Locate and identify every blood parasite.
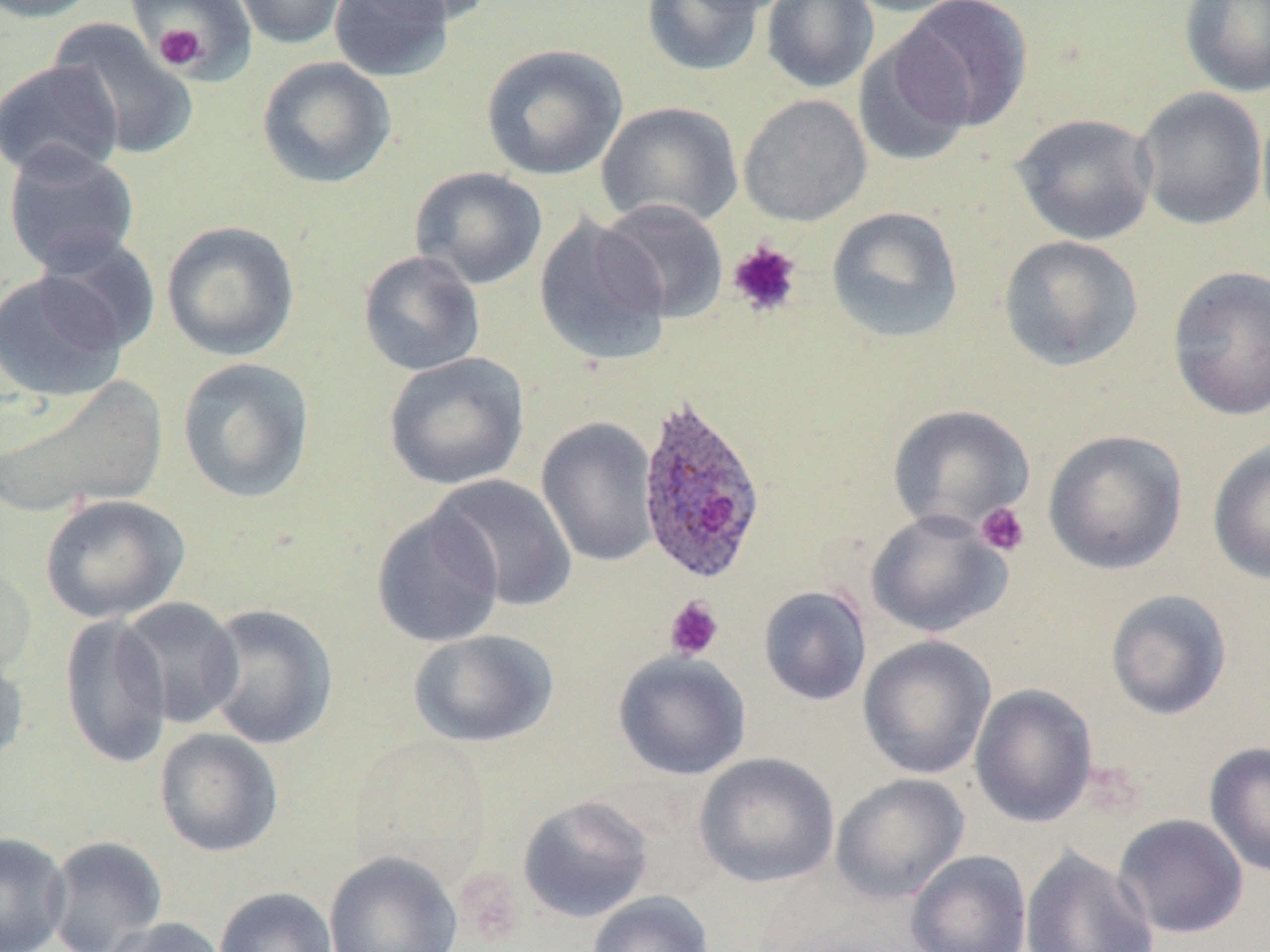

Approximate bounding boxes as (x1, y1, x2, y2) in pixels.
Plasmodium ovale-infected red blood cells: (636, 396, 767, 585).
No Plasmodium falciparum, Plasmodium malariae, Plasmodium vivax, Babesia divergens, or Trypanosoma brucei observed.

Platelet locations: (154, 23, 207, 71), (727, 240, 802, 318), (976, 502, 1031, 557), (664, 596, 724, 661). Uninfected red blood cell locations: (0, 0, 103, 23), (231, 0, 350, 50), (329, 0, 456, 82), (357, 0, 497, 27), (640, 0, 766, 78), (681, 0, 797, 16), (760, 0, 879, 93), (842, 0, 975, 17), (1178, 0, 1270, 98), (895, 1, 1034, 132), (136, 4, 248, 81), (47, 18, 200, 162), (853, 33, 974, 169), (479, 44, 628, 182), (256, 56, 397, 189), (0, 60, 124, 182), (1134, 87, 1268, 231), (738, 94, 872, 226), (597, 101, 744, 230), (1256, 101, 1270, 234), (1011, 112, 1158, 246), (2, 142, 141, 276), (409, 166, 548, 290), (596, 198, 729, 323), (826, 206, 964, 344), (533, 215, 672, 366), (161, 220, 300, 361), (35, 232, 161, 355), (998, 235, 1143, 372), (358, 250, 486, 376), (1167, 266, 1270, 420), (0, 271, 129, 402), (383, 352, 530, 491), (176, 357, 315, 504), (1, 376, 168, 517), (887, 403, 1034, 534), (536, 416, 661, 569), (1043, 429, 1188, 575), (1207, 440, 1270, 585), (427, 473, 579, 613), (39, 494, 190, 623), (370, 507, 505, 648), (866, 509, 1012, 638), (758, 585, 872, 706), (1105, 589, 1233, 720), (115, 596, 245, 729), (200, 603, 338, 750), (58, 613, 173, 770), (408, 628, 558, 749), (857, 635, 996, 780), (0, 650, 30, 767), (613, 650, 752, 781), (970, 684, 1098, 827), (154, 727, 284, 857), (349, 734, 492, 884), (1204, 741, 1270, 878), (694, 752, 840, 888), (831, 773, 969, 903), (517, 795, 654, 923), (1113, 813, 1249, 939), (0, 830, 71, 952), (43, 836, 169, 952), (1020, 847, 1159, 952), (905, 849, 1032, 952), (323, 850, 463, 952), (214, 887, 338, 952), (587, 891, 715, 952), (101, 917, 230, 952). Slide-level diagnosis: Plasmodium ovale. 1000x magnification. One field of a larger specimen. May-Grünwald-Giemsa stain. Light microscopy. Thin blood smear. Image is 1270×952 pixels.